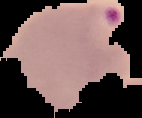
preparation: thin blood smear
result: Plasmodium parasites identified
image_size: 142×118 pixels
image_type: segmented cell region on a black background